Comment on the morphology of the red blood cells.
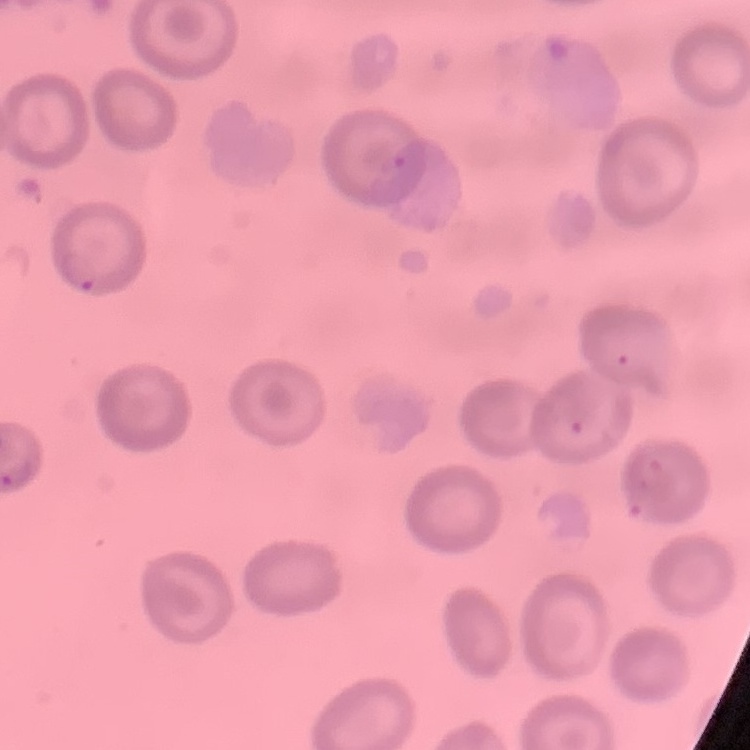
No rouleaux formation.

{
  "stain": "Field's or Giemsa",
  "image_type": "square crop of a larger photomicrograph",
  "preparation": "thin blood smear"
}